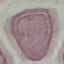

Summary:
  - Result: no malaria parasites detected
  - Stain: Giemsa
  - Image type: cell patch, automatically extracted from a larger field of view and resized to 64 × 64 pixels
  - Preparation: thin blood film
  - Capture: smartphone through the microscope eyepiece